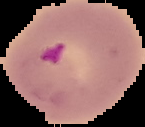

Segmented cell region on a black background. Image is 145×127 pixels. Result: malaria parasites identified. From a thin blood smear.